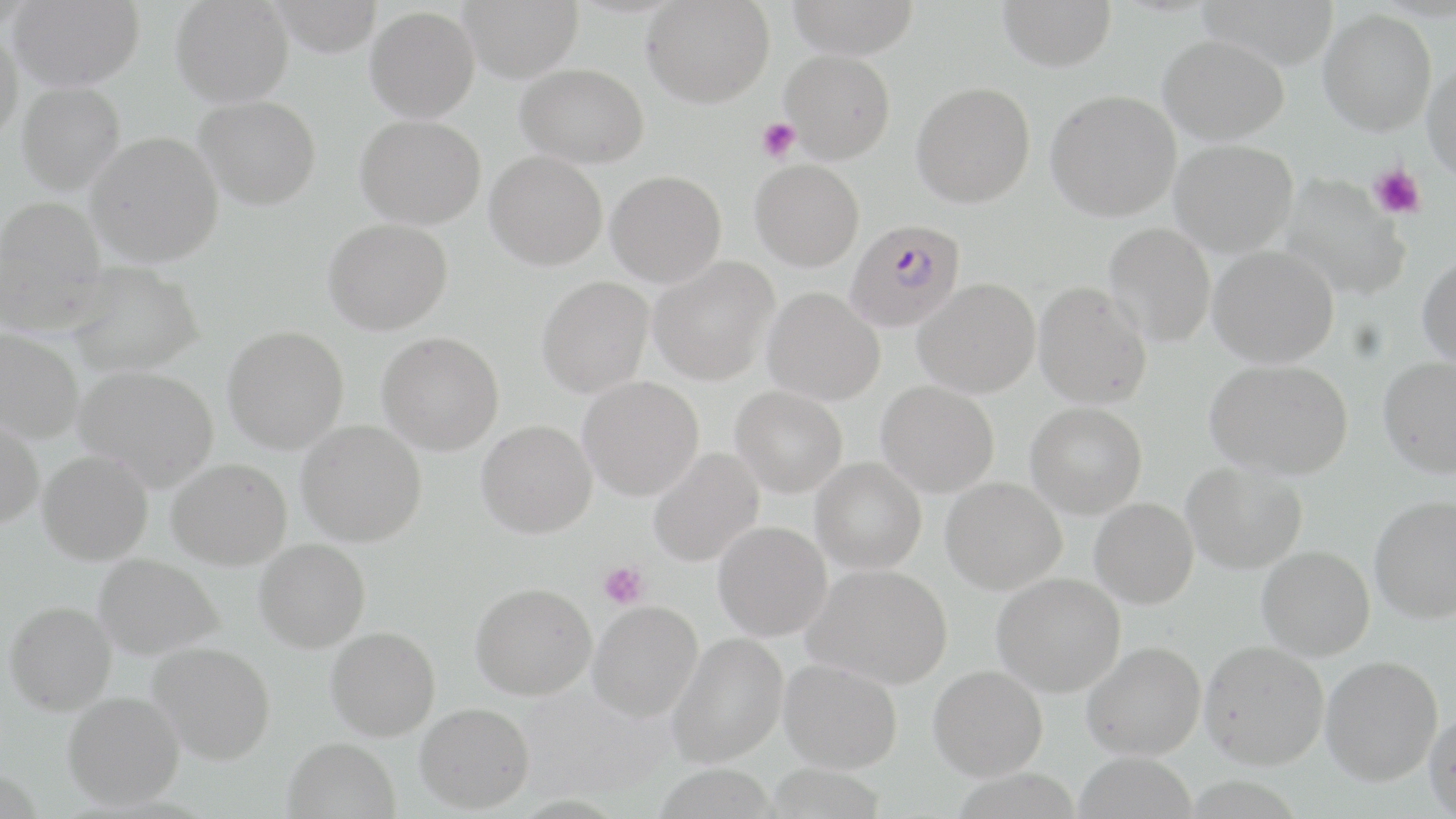

slide-level diagnosis = Plasmodium falciparum
image size = 1456×819 pixels
uninfected red blood cell locations = approximate bounding boxes as (x1, y1, x2, y2) in pixels: (7, 0, 145, 90), (171, 0, 294, 107), (458, 0, 583, 82), (642, 0, 774, 107), (785, 0, 921, 58), (998, 0, 1117, 71), (1195, 0, 1339, 68), (366, 6, 480, 122), (1319, 8, 1437, 136), (0, 24, 24, 143), (1158, 33, 1290, 144), (780, 49, 895, 163), (1422, 61, 1456, 186), (516, 63, 649, 168), (911, 81, 1036, 207), (16, 82, 125, 194), (1046, 90, 1181, 221), (194, 95, 321, 209), (355, 114, 486, 229), (86, 132, 224, 266), (1170, 139, 1298, 257), (485, 150, 608, 270), (750, 160, 864, 271), (606, 171, 727, 287), (1279, 174, 1410, 301), (0, 196, 107, 332), (322, 218, 453, 335), (1103, 223, 1216, 348), (1208, 245, 1339, 368), (1417, 252, 1456, 369), (649, 256, 779, 385), (63, 261, 204, 377), (536, 276, 653, 398), (914, 279, 1041, 398), (1034, 281, 1152, 409), (763, 287, 885, 405), (223, 325, 349, 454), (0, 327, 84, 443), (377, 332, 504, 455), (1378, 356, 1456, 477), (1204, 359, 1353, 480), (73, 366, 218, 490), (578, 376, 704, 500), (876, 382, 999, 497), (731, 386, 848, 498), (1026, 402, 1147, 518), (0, 412, 45, 530), (297, 420, 427, 547), (477, 420, 597, 538), (648, 448, 764, 568), (38, 450, 153, 565), (167, 458, 292, 569), (811, 458, 926, 574), (1182, 461, 1308, 574), (941, 477, 1067, 594), (1369, 495, 1456, 623), (1090, 498, 1198, 608), (713, 521, 831, 640), (254, 539, 370, 652), (1257, 545, 1375, 661), (94, 553, 224, 659), (802, 564, 952, 689), (991, 573, 1125, 697), (470, 582, 597, 700), (4, 601, 117, 715), (589, 601, 703, 720), (326, 626, 440, 741), (668, 632, 788, 768), (1200, 641, 1330, 770), (149, 642, 276, 765), (1081, 642, 1206, 760), (1320, 654, 1443, 786), (779, 658, 903, 773), (929, 665, 1048, 780), (63, 691, 184, 809), (416, 702, 535, 812), (1424, 707, 1456, 817), (283, 737, 400, 819), (1074, 751, 1197, 819)
field of view = single
magnification = 1000x
Plasmodium falciparum-infected red blood cell locations = approximate bounding boxes as (x1, y1, x2, y2) in pixels: (845, 218, 965, 332)
stain = May-Grünwald-Giemsa
modality = optical microscopy
preparation = thin blood film
platelet locations = approximate bounding boxes as (x1, y1, x2, y2) in pixels: (757, 117, 800, 162), (1369, 165, 1426, 220), (597, 561, 649, 610)